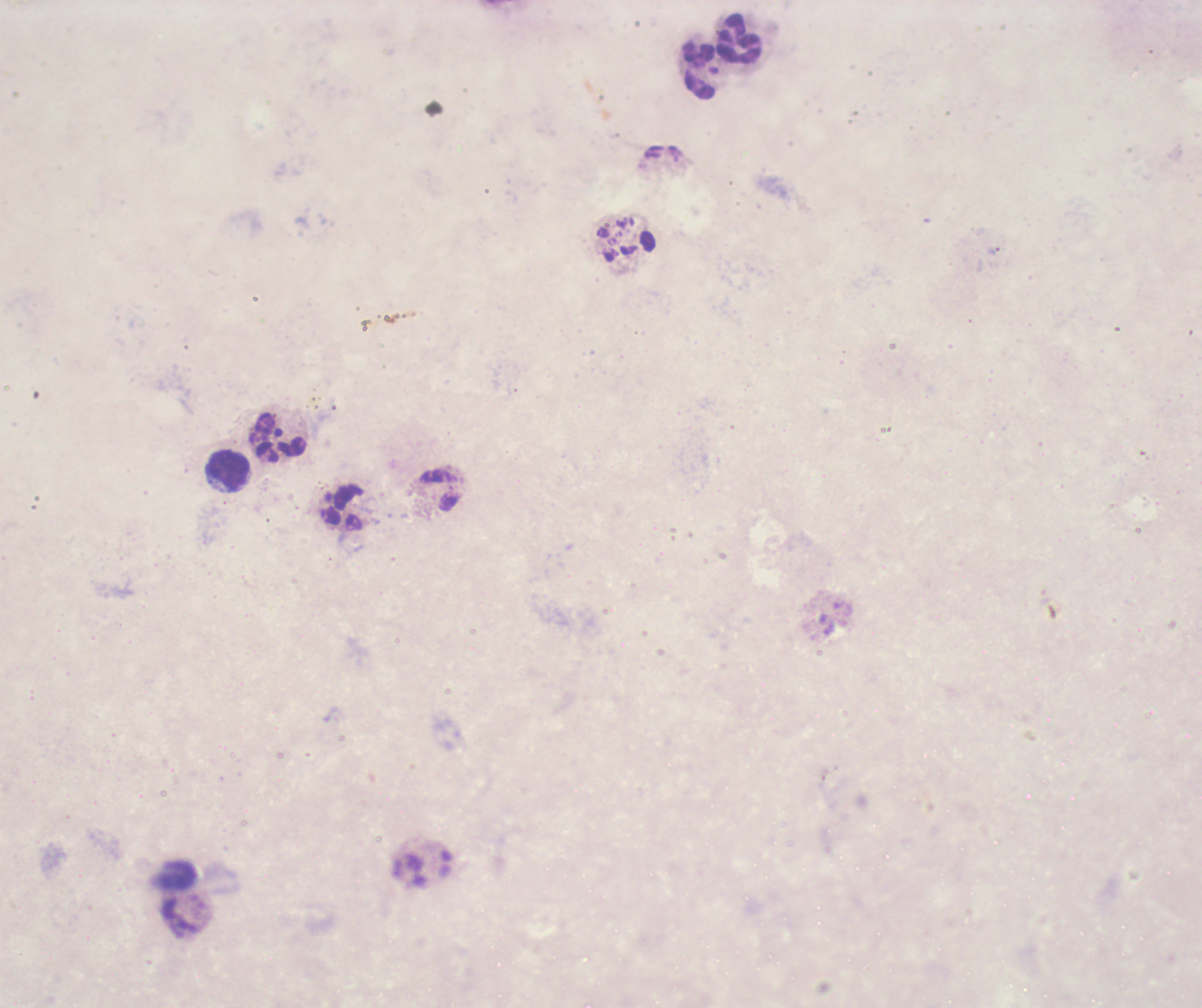

Approximate centers as (x, y) in pixels.
Summary:
  - Leukocyte locations: (738, 38), (699, 71), (279, 437), (230, 472), (440, 490)
  - Image size: 1202×1008 pixels
  - Stain: Romanowsky
  - Result: negative for Plasmodium parasites
  - Preparation: thick blood smear
  - Background quality: unsatisfactory
  - Magnification: 100x
  - Context: previously used in an actual diagnosis
  - Field of view: one from this slide
  - Coloration quality: bad